Point out each Plasmodium parasite.
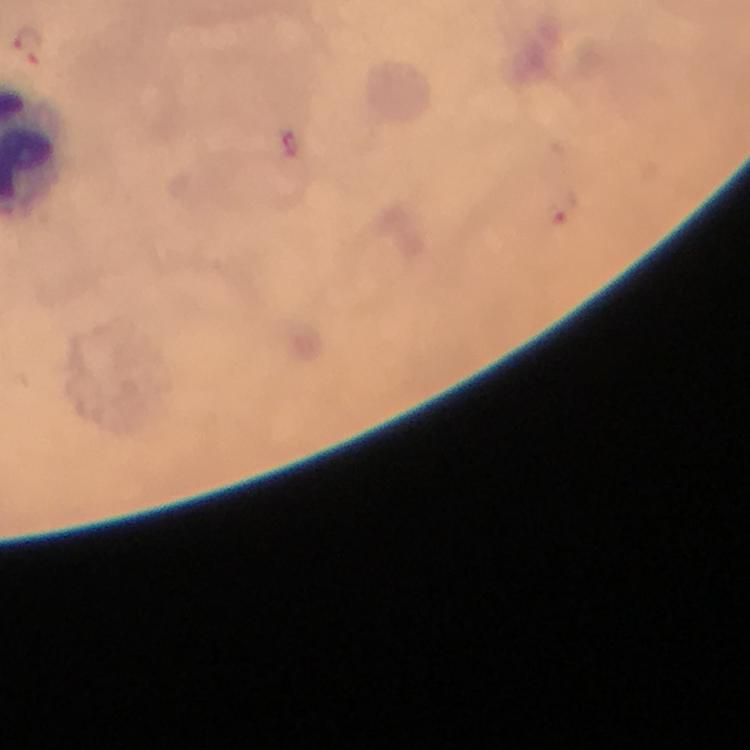
Approximate centers as [x, y] in pixels.
Plasmodium parasites: [30, 45], [563, 208].

Summary:
  - Image size: 750×750 pixels
  - Preparation: thick blood smear
  - Context: from a diagnostic examination for malaria
  - Capture: smartphone photograph through a microscope
  - Immersion oil: applied
  - Cropped from: one field of view
  - Magnification: 100x
  - Stain: Giemsa